Identify the blood parasite species.
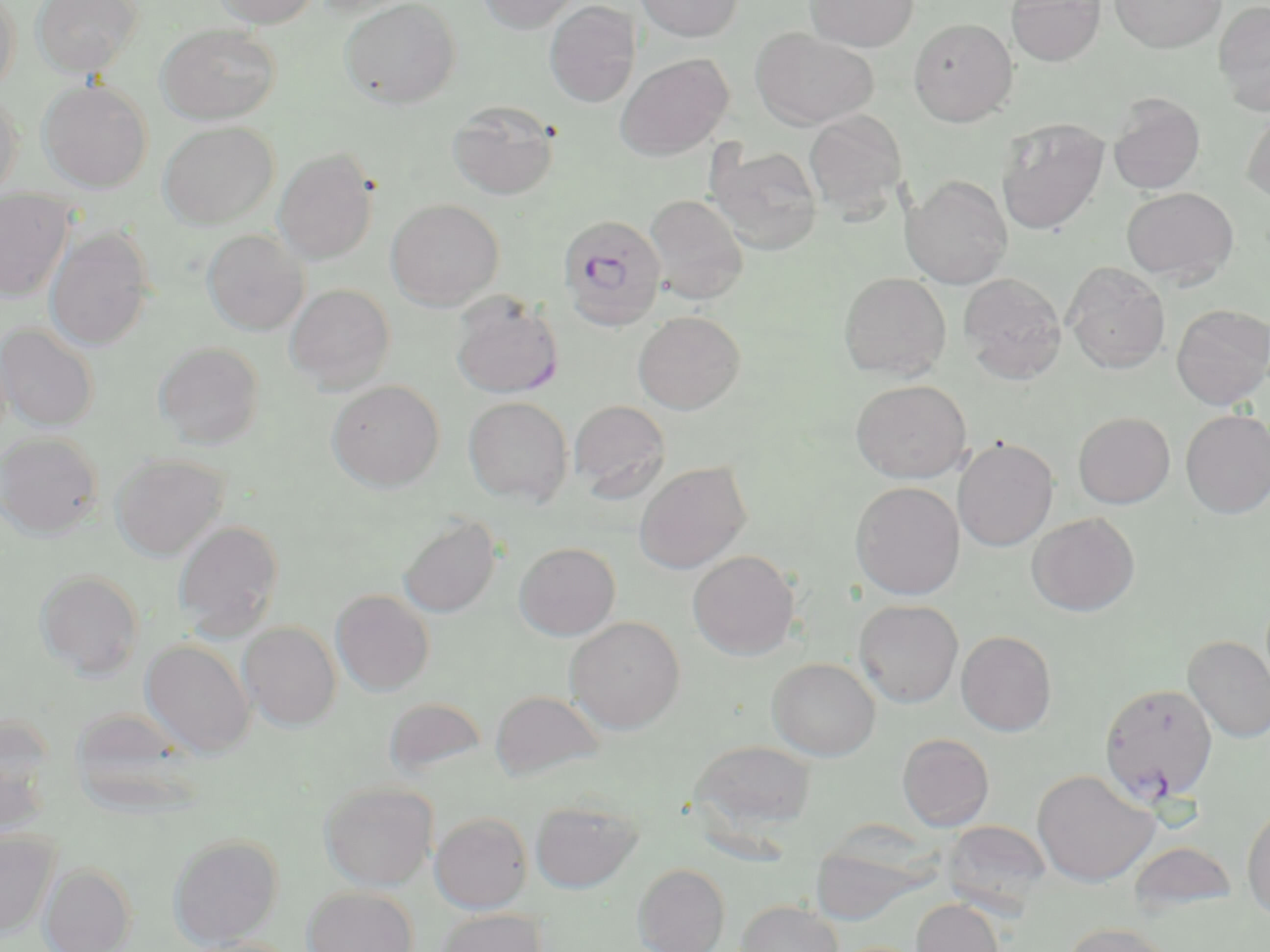

Plasmodium falciparum.

Approximate bounding boxes as named x1/y1/x2/y2 corners in pixels. Uninfected red blood cell locations: (x1=0, y1=0, x2=21, y2=96), (x1=31, y1=0, x2=142, y2=78), (x1=212, y1=0, x2=321, y2=27), (x1=311, y1=0, x2=421, y2=18), (x1=340, y1=0, x2=461, y2=108), (x1=477, y1=0, x2=581, y2=33), (x1=635, y1=0, x2=743, y2=42), (x1=805, y1=0, x2=918, y2=51), (x1=1006, y1=0, x2=1106, y2=65), (x1=1109, y1=0, x2=1226, y2=53), (x1=1213, y1=0, x2=1270, y2=116), (x1=544, y1=1, x2=640, y2=107), (x1=908, y1=18, x2=1018, y2=126), (x1=157, y1=24, x2=280, y2=124), (x1=751, y1=28, x2=879, y2=129), (x1=615, y1=53, x2=733, y2=161), (x1=38, y1=79, x2=153, y2=192), (x1=0, y1=90, x2=23, y2=202), (x1=1108, y1=94, x2=1206, y2=195), (x1=447, y1=100, x2=560, y2=201), (x1=1241, y1=107, x2=1270, y2=204), (x1=803, y1=110, x2=907, y2=218), (x1=995, y1=118, x2=1109, y2=235), (x1=158, y1=121, x2=279, y2=229), (x1=706, y1=143, x2=823, y2=255), (x1=273, y1=147, x2=379, y2=264), (x1=902, y1=175, x2=1013, y2=289), (x1=1121, y1=187, x2=1239, y2=285), (x1=0, y1=189, x2=74, y2=302), (x1=644, y1=195, x2=748, y2=305), (x1=386, y1=199, x2=504, y2=309), (x1=45, y1=227, x2=155, y2=351), (x1=202, y1=229, x2=309, y2=336), (x1=1064, y1=262, x2=1170, y2=373), (x1=838, y1=272, x2=951, y2=380), (x1=958, y1=273, x2=1067, y2=384), (x1=286, y1=284, x2=395, y2=394), (x1=450, y1=292, x2=564, y2=399), (x1=1171, y1=304, x2=1270, y2=409), (x1=633, y1=311, x2=745, y2=414), (x1=0, y1=323, x2=99, y2=431), (x1=154, y1=342, x2=264, y2=448), (x1=851, y1=379, x2=971, y2=483), (x1=327, y1=380, x2=445, y2=491), (x1=463, y1=396, x2=574, y2=506), (x1=569, y1=400, x2=670, y2=501), (x1=1180, y1=409, x2=1270, y2=518), (x1=1073, y1=411, x2=1175, y2=508), (x1=0, y1=432, x2=103, y2=539), (x1=954, y1=438, x2=1058, y2=551), (x1=111, y1=453, x2=229, y2=560), (x1=634, y1=461, x2=751, y2=574), (x1=850, y1=481, x2=965, y2=600), (x1=398, y1=513, x2=503, y2=618), (x1=1027, y1=513, x2=1140, y2=616), (x1=173, y1=520, x2=285, y2=639), (x1=514, y1=542, x2=621, y2=640), (x1=687, y1=550, x2=800, y2=659), (x1=35, y1=569, x2=144, y2=680), (x1=331, y1=589, x2=435, y2=696), (x1=854, y1=599, x2=964, y2=707), (x1=565, y1=616, x2=686, y2=733), (x1=238, y1=621, x2=342, y2=730), (x1=956, y1=630, x2=1057, y2=736), (x1=1182, y1=635, x2=1270, y2=743), (x1=141, y1=639, x2=255, y2=758), (x1=767, y1=657, x2=881, y2=761), (x1=490, y1=690, x2=605, y2=781), (x1=384, y1=696, x2=487, y2=778), (x1=0, y1=717, x2=56, y2=836), (x1=897, y1=733, x2=994, y2=831), (x1=689, y1=740, x2=817, y2=833), (x1=1031, y1=769, x2=1159, y2=887), (x1=319, y1=781, x2=438, y2=890), (x1=530, y1=799, x2=643, y2=893), (x1=1242, y1=801, x2=1270, y2=921), (x1=430, y1=812, x2=532, y2=913), (x1=942, y1=820, x2=1052, y2=914), (x1=0, y1=830, x2=59, y2=937), (x1=168, y1=833, x2=283, y2=948), (x1=1127, y1=841, x2=1237, y2=916), (x1=40, y1=862, x2=136, y2=952), (x1=633, y1=863, x2=730, y2=952), (x1=303, y1=886, x2=418, y2=952), (x1=912, y1=899, x2=1005, y2=952), (x1=735, y1=900, x2=843, y2=952), (x1=434, y1=908, x2=547, y2=952), (x1=1063, y1=922, x2=1178, y2=952). Plasmodium falciparum-infected red blood cell locations: (x1=557, y1=214, x2=667, y2=331), (x1=1100, y1=682, x2=1218, y2=805). 1000x magnification. Image is 1270×952 pixels. Optical microscopy. May-Grünwald-Giemsa-stained preparation. Thin blood film. Single field of view.